State which cell type is depicted.
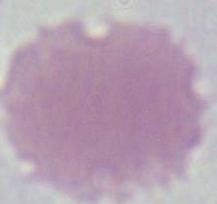
An erythrocyte.

modality = micrograph
magnification = 1000x